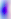

magnification = 400x
identification = Toxoplasma gondii
modality = photomicrograph